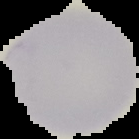
image_size: 139×139 pixels
image_type: cell region segmented out of the field of view; surrounding area masked to black
preparation: thin blood film
malaria_status: parasitized